Identify the parasite.
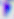

This is Toxoplasma gondii.

Summary:
  - Magnification: 400x
  - Modality: micrograph